Point out each leukocyte.
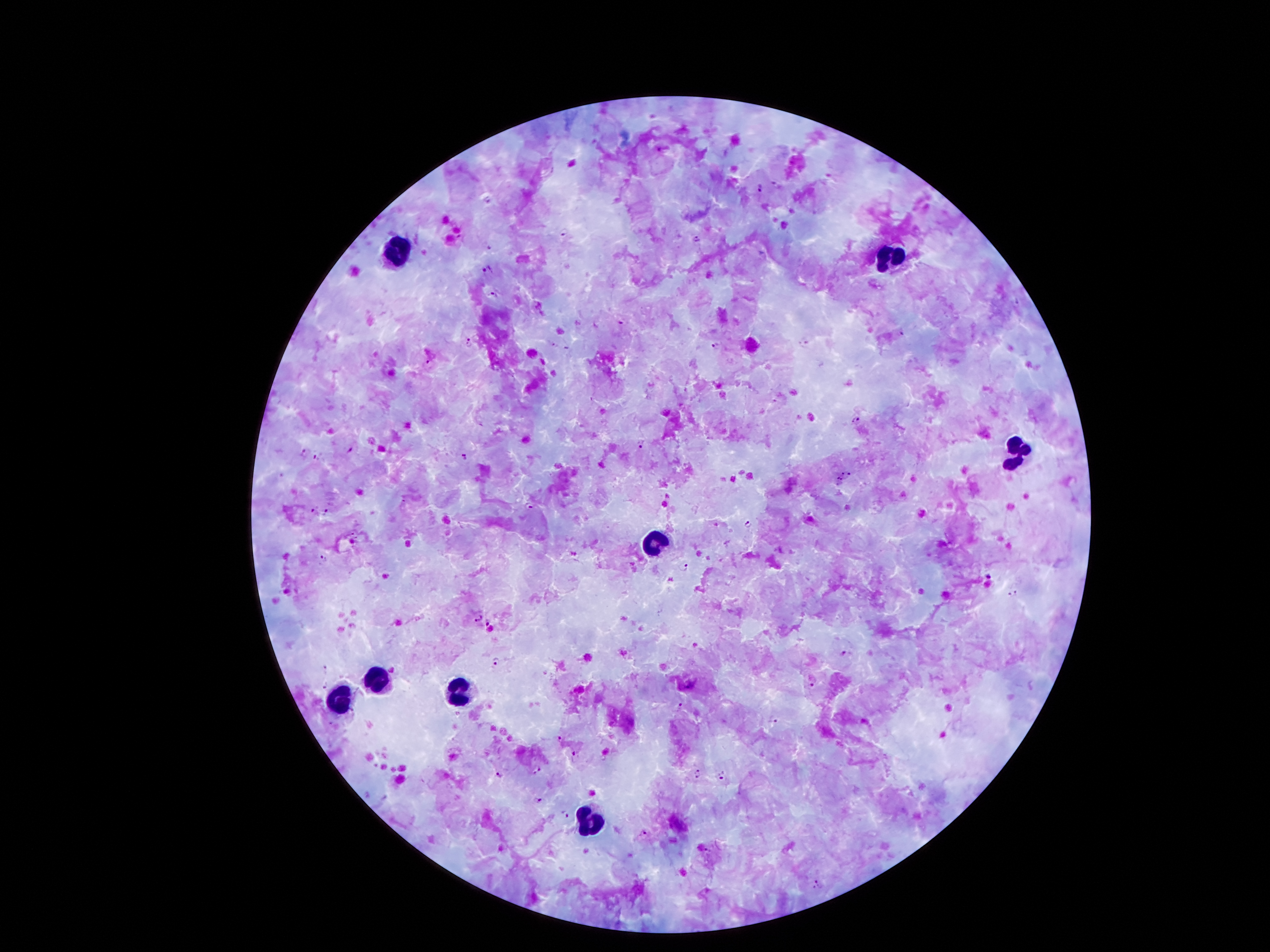
Approximate object centers, in pixels from the top-left corner.
Leukocytes: (x=396, y=252), (x=889, y=257), (x=1017, y=448), (x=658, y=544), (x=370, y=681), (x=461, y=693), (x=340, y=702), (x=592, y=824).

Summary:
  - Malaria parasite locations: (x=759, y=188), (x=564, y=231), (x=696, y=237), (x=490, y=248), (x=488, y=270), (x=494, y=294), (x=621, y=323), (x=468, y=341), (x=805, y=343), (x=717, y=345), (x=428, y=361), (x=855, y=419), (x=643, y=443), (x=350, y=447), (x=303, y=452), (x=464, y=455), (x=317, y=456), (x=841, y=472), (x=848, y=476), (x=839, y=479), (x=530, y=506), (x=325, y=510), (x=311, y=511), (x=749, y=525), (x=323, y=557), (x=684, y=567), (x=988, y=576), (x=1014, y=592), (x=477, y=618), (x=487, y=623), (x=845, y=652), (x=497, y=661), (x=323, y=668), (x=813, y=684), (x=326, y=685), (x=680, y=705), (x=774, y=718), (x=331, y=722), (x=561, y=739), (x=575, y=757), (x=537, y=768), (x=697, y=774), (x=499, y=775), (x=722, y=775), (x=537, y=799), (x=564, y=815), (x=644, y=832), (x=817, y=885)
  - Patient malaria status: infected with Plasmodium falciparum
  - Magnification: 100x
  - Preparation: thick blood film
  - Stain: Giemsa
  - Image size: 1270×952 pixels
  - Field of view: single
  - Capture: smartphone through the microscope eyepiece